State which cell type is depicted.
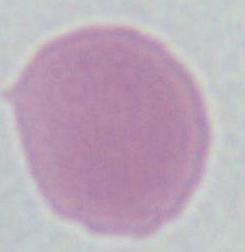
This is an erythrocyte.

Summary:
  - Magnification: 1000x
  - Modality: micrograph